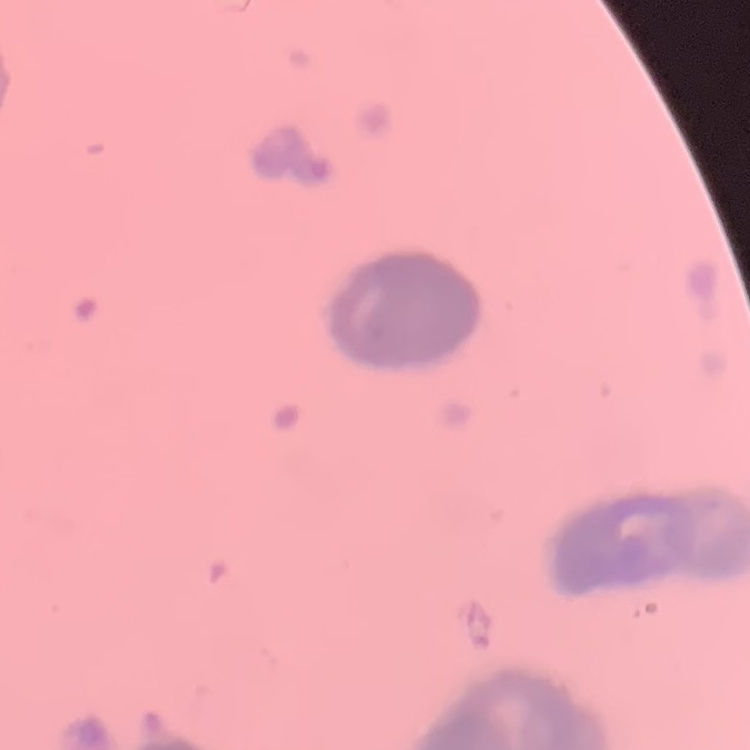

Summary:
  - Red blood cell morphology: rouleaux formation
  - Image type: one tile cut from a larger photomicrograph
  - Stain: Field's or Giemsa
  - Preparation: thin peripheral smear